Assess this cell for malaria.
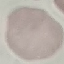
Uninfected.

Thin blood smear. Photographed with a smartphone camera at the microscope eyepiece. Giemsa-stained preparation. Automatically extracted cell patch, resized to 64 × 64 pixels.